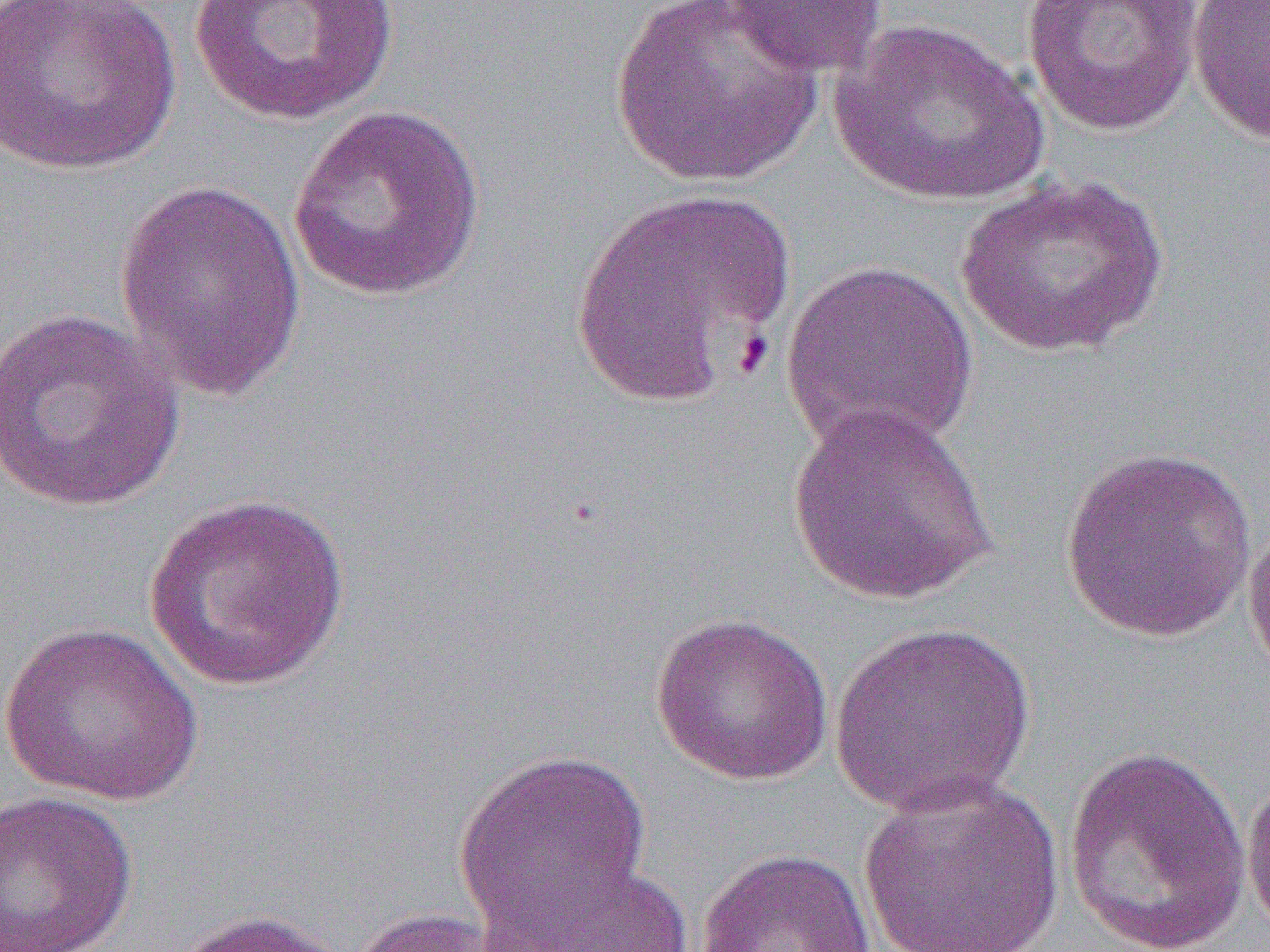

Summary:
  - Coordinate format: approximate bounding boxes as (x1, y1, x2, y2) in pixels
  - Uninfected red blood cell locations: (0, 0, 181, 176), (186, 0, 401, 125), (609, 0, 824, 189), (719, 0, 890, 78), (1021, 0, 1205, 137), (1187, 0, 1270, 148), (832, 18, 1050, 207), (287, 104, 486, 302), (955, 173, 1169, 359), (113, 177, 309, 404), (568, 186, 796, 407), (781, 258, 977, 457), (0, 306, 187, 513), (783, 402, 1001, 608), (1059, 446, 1258, 644), (142, 493, 352, 693), (1242, 515, 1270, 687), (649, 612, 834, 786), (0, 621, 205, 805), (827, 621, 1036, 818), (453, 747, 652, 937), (1063, 747, 1253, 952), (1241, 772, 1270, 943), (857, 774, 1065, 951), (0, 790, 140, 951), (696, 846, 878, 952), (479, 862, 692, 952), (346, 906, 520, 952), (165, 908, 355, 952)
  - Slide-level diagnosis: Plasmodium falciparum
  - Modality: optical microscopy
  - Field of view: one of a larger specimen
  - Magnification: 1000x
  - Image size: 1270×952 pixels
  - Preparation: thin blood smear